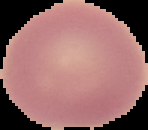

Cell region segmented out of the field of view; the surrounding area is masked to black. From a thin blood smear. Malaria status: uninfected. Image is 148×130 pixels.